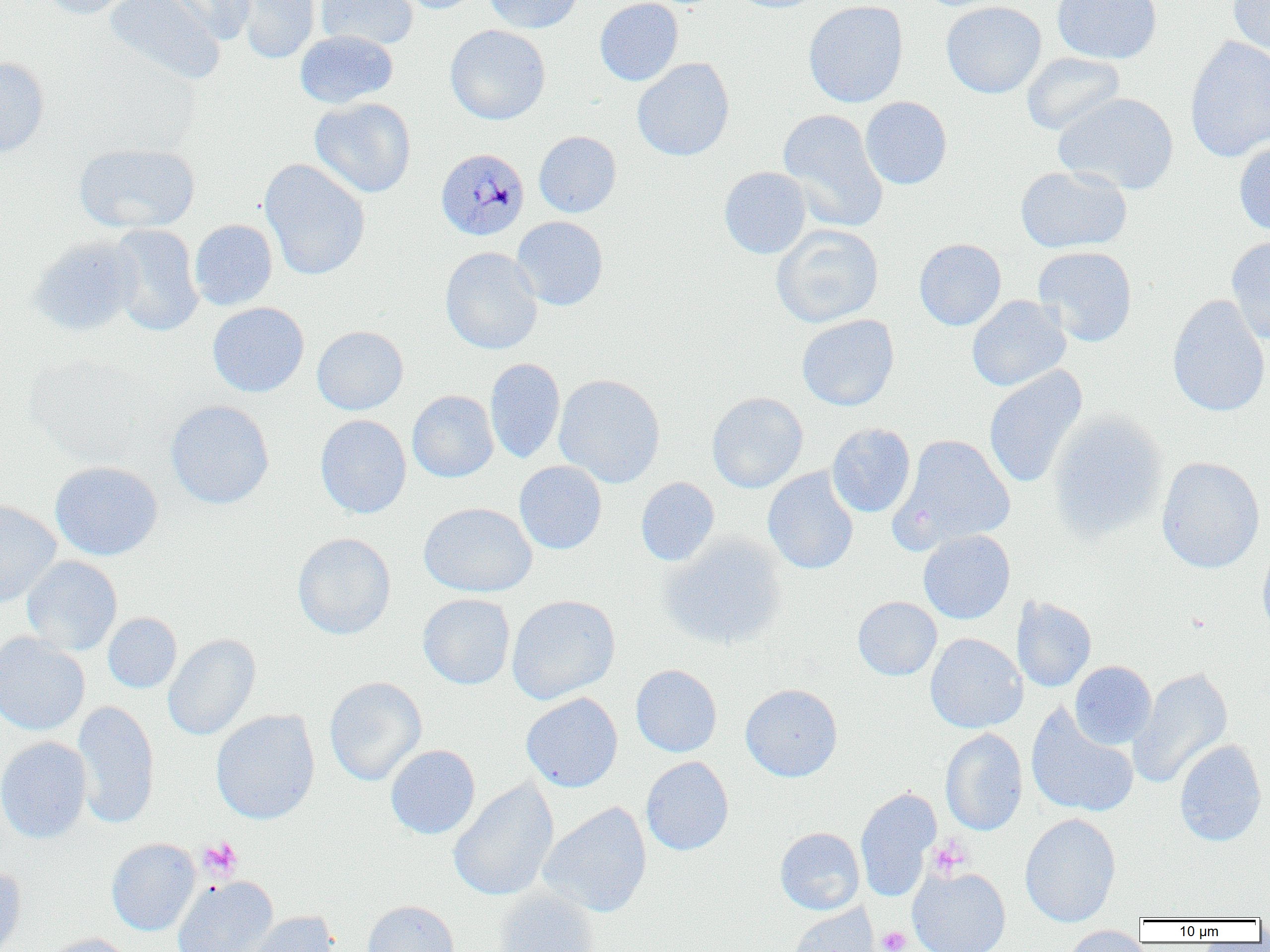
Approximate bounding boxes as [x1, y1, x2, y2] in pixels. Uninfected red blood cell locations: [37, 0, 139, 19], [104, 0, 225, 84], [157, 0, 254, 45], [233, 0, 320, 64], [315, 0, 418, 51], [388, 0, 485, 14], [483, 0, 584, 33], [595, 0, 683, 86], [728, 0, 828, 13], [803, 0, 908, 108], [1052, 0, 1162, 64], [940, 1, 1047, 98], [1227, 1, 1270, 55], [445, 25, 550, 125], [295, 30, 398, 109], [1185, 36, 1270, 162], [1021, 52, 1125, 136], [0, 56, 50, 159], [632, 58, 735, 161], [1053, 92, 1178, 194], [309, 97, 417, 198], [860, 97, 952, 189], [778, 109, 888, 233], [534, 131, 622, 217], [1234, 140, 1270, 236], [74, 142, 200, 234], [259, 159, 370, 281], [1015, 165, 1132, 253], [719, 166, 812, 259], [511, 216, 608, 310], [189, 219, 278, 310], [107, 224, 204, 337], [771, 224, 884, 327], [1226, 234, 1270, 343], [29, 236, 142, 337], [914, 238, 1006, 330], [1033, 246, 1138, 347], [440, 247, 543, 355], [1166, 294, 1270, 417], [966, 295, 1071, 392], [207, 302, 309, 397], [796, 314, 899, 411], [312, 325, 408, 415], [484, 358, 566, 464], [984, 365, 1087, 489], [554, 374, 665, 488], [407, 390, 499, 482], [707, 392, 808, 493], [165, 400, 275, 509], [1047, 410, 1169, 543], [315, 414, 411, 519], [827, 423, 916, 518], [892, 434, 1016, 551], [1156, 456, 1265, 574], [50, 461, 163, 561], [514, 461, 607, 554], [763, 466, 859, 575], [636, 477, 720, 566], [0, 499, 61, 607], [418, 502, 537, 597], [918, 530, 1015, 624], [292, 532, 396, 640], [658, 532, 788, 650], [1257, 542, 1270, 647], [21, 556, 122, 656], [418, 594, 515, 689], [506, 594, 620, 705], [1011, 596, 1096, 692], [853, 597, 942, 681], [103, 612, 182, 693], [0, 632, 90, 736], [925, 633, 1027, 733], [162, 634, 261, 741], [1070, 661, 1156, 748], [631, 665, 722, 757], [1129, 667, 1233, 790], [324, 676, 427, 786], [740, 683, 842, 782], [520, 693, 623, 792], [72, 700, 159, 829], [1026, 705, 1139, 818], [210, 710, 320, 824], [940, 728, 1027, 836], [0, 736, 92, 844], [1174, 739, 1267, 846], [385, 744, 480, 839], [641, 756, 734, 856], [448, 779, 559, 901], [855, 787, 941, 901], [539, 802, 652, 918], [1020, 813, 1121, 928], [775, 827, 865, 914], [106, 838, 201, 936], [0, 866, 26, 952], [907, 866, 1011, 952], [172, 876, 278, 952], [492, 888, 600, 952], [362, 899, 458, 952], [786, 904, 881, 952], [240, 910, 341, 952], [1059, 925, 1150, 952], [39, 933, 135, 952]. Plasmodium malariae-infected red blood cell locations: [436, 147, 530, 240]. Platelet locations: [198, 836, 242, 880], [927, 837, 972, 878], [877, 926, 911, 952]. Slide-level diagnosis: Plasmodium malariae. Light microscopy. One field of a larger specimen. Captured at 1000x magnification. Image is 1270×952 pixels. Thin blood film.